Locate every Plasmodium falciparum-infected red blood cell.
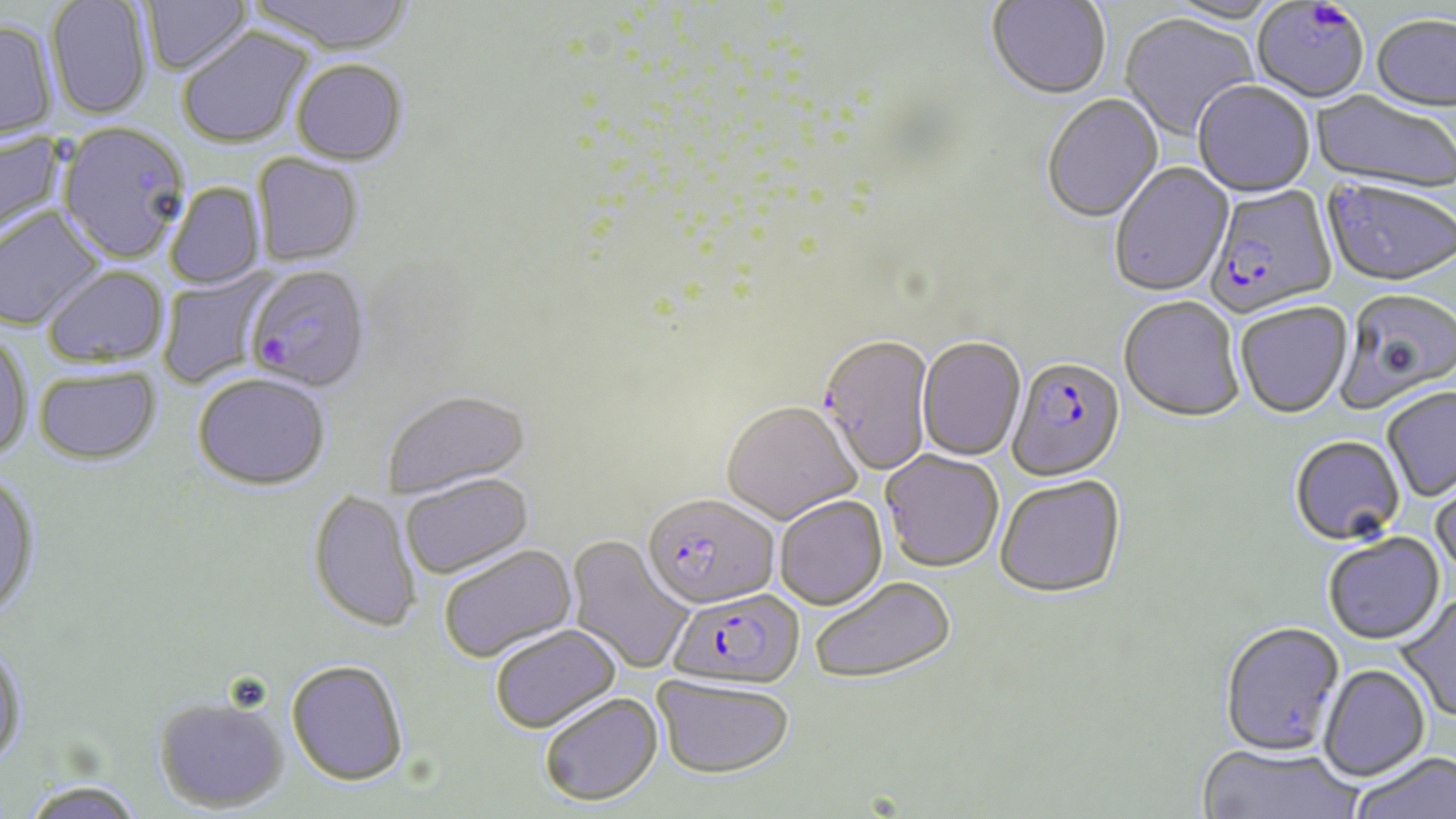

Approximate bounding boxes as (x1,y1)-(x2,y2) corner pairs in pixels.
Plasmodium falciparum-infected red blood cells: (1205,185)-(1338,319), (244,265)-(370,393), (817,334)-(936,477), (1007,357)-(1126,482), (642,491)-(779,608), (665,587)-(805,691).

Uninfected red blood cell locations: (140,0)-(252,77), (245,0)-(417,56), (46,1)-(153,121), (987,1)-(1111,102), (1251,3)-(1369,105), (1118,15)-(1257,143), (1371,17)-(1456,115), (0,20)-(58,141), (177,28)-(313,149), (290,59)-(409,166), (1193,83)-(1315,200), (1308,91)-(1456,197), (1041,95)-(1164,225), (56,122)-(191,264), (0,130)-(65,241), (252,154)-(364,266), (1110,162)-(1235,299), (166,182)-(265,289), (1321,182)-(1456,291), (0,206)-(107,332), (43,266)-(168,369), (159,268)-(276,387), (1335,290)-(1455,413), (1118,298)-(1244,424), (1235,304)-(1353,420), (0,332)-(33,463), (918,337)-(1026,462), (32,365)-(162,466), (192,372)-(331,490), (380,388)-(532,498), (1382,388)-(1456,503), (721,400)-(862,524), (1289,437)-(1405,548), (880,450)-(1003,573), (1430,467)-(1456,589), (0,471)-(42,618), (399,472)-(533,579), (995,475)-(1127,601), (308,488)-(423,632), (774,495)-(886,610), (567,534)-(695,675), (1323,534)-(1445,647), (439,543)-(577,663), (809,575)-(957,684), (1394,595)-(1456,724), (1219,622)-(1346,759), (488,623)-(622,733), (0,640)-(28,768), (286,658)-(410,786), (1319,666)-(1430,783), (653,675)-(794,778), (538,691)-(663,806), (153,693)-(290,812), (1194,745)-(1363,819), (1350,753)-(1455,819), (17,779)-(148,818). Platelet locations: (1309,2)-(1343,30). Slide-level diagnosis: Plasmodium falciparum. Image is 1456×819 pixels. Captured at 1000x magnification. May-Grünwald-Giemsa stain. Thin blood film. Optical microscopy. One field of a larger specimen.